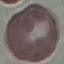
result: no malaria parasites detected
preparation: thin smear
image_type: automatically extracted cell patch, resized to 64 × 64 pixels
capture: smartphone through the microscope eyepiece
stain: Giemsa